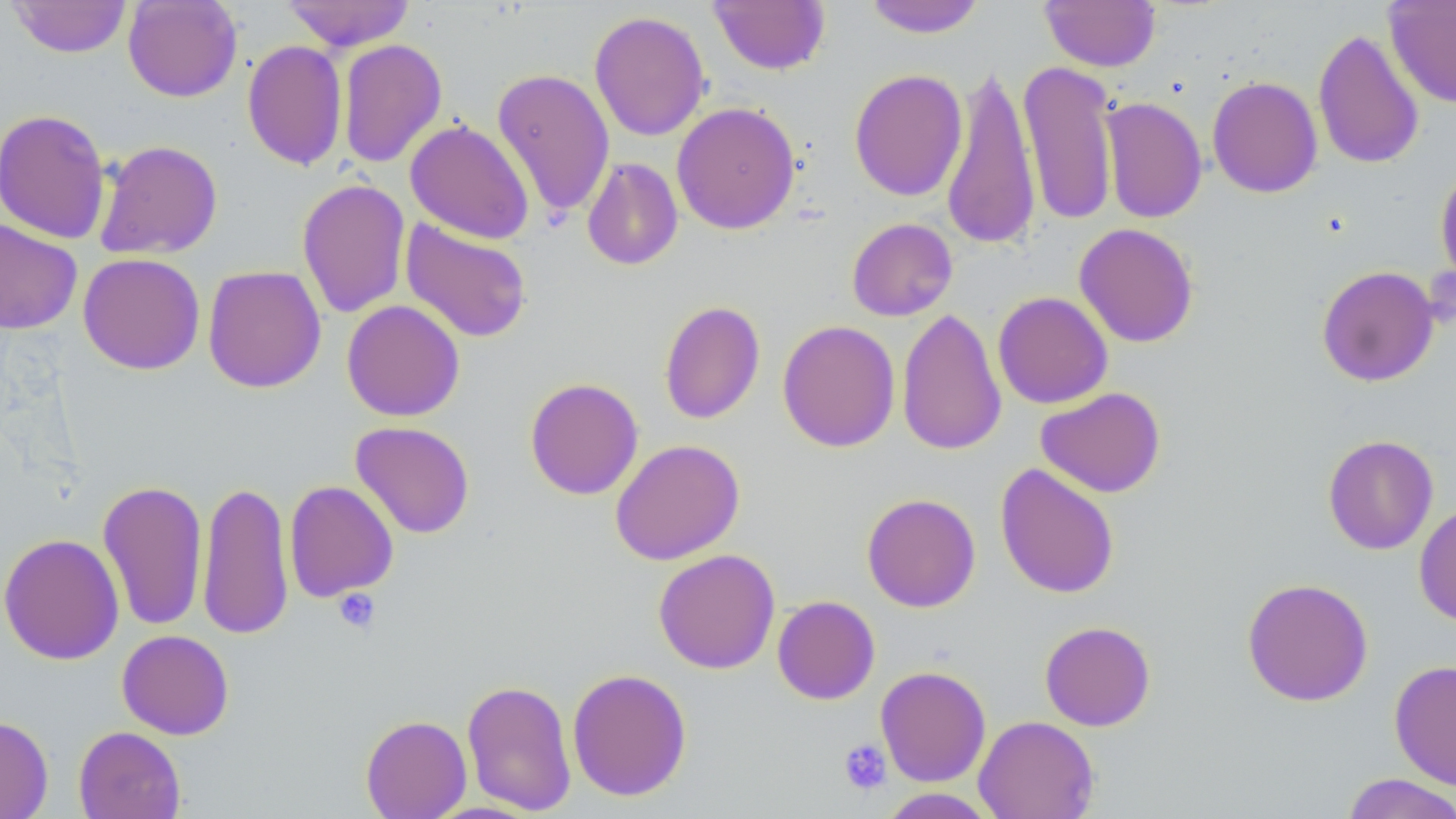 Approximate bounding boxes as (x1, y1, x2, y2) in pixels. Platelet locations: (332, 587, 380, 633), (838, 738, 892, 795). Uninfected red blood cell locations: (8, 0, 132, 58), (122, 0, 242, 102), (282, 0, 415, 51), (862, 0, 987, 38), (1040, 0, 1161, 71), (1384, 0, 1456, 108), (708, 1, 831, 75), (589, 11, 710, 141), (1312, 27, 1425, 170), (337, 38, 447, 169), (242, 40, 348, 171), (1018, 58, 1119, 227), (941, 63, 1041, 251), (492, 67, 615, 221), (848, 68, 967, 201), (1207, 76, 1323, 198), (1100, 96, 1207, 224), (672, 101, 800, 234), (0, 109, 112, 244), (405, 119, 535, 244), (94, 140, 223, 260), (581, 157, 683, 271), (1435, 164, 1456, 290), (297, 178, 411, 319), (846, 217, 958, 322), (0, 218, 83, 334), (400, 218, 533, 344), (1074, 223, 1199, 348), (78, 253, 205, 375), (202, 265, 326, 393), (1316, 265, 1440, 387), (992, 291, 1113, 409), (341, 300, 465, 421), (658, 300, 765, 425), (897, 307, 1007, 456), (777, 320, 900, 453), (524, 377, 644, 500), (1036, 387, 1166, 498), (350, 421, 475, 539), (1323, 434, 1438, 554), (610, 439, 745, 565), (995, 463, 1120, 599), (97, 479, 208, 631), (197, 480, 294, 641), (284, 480, 399, 602), (861, 493, 981, 612), (1414, 503, 1456, 627), (0, 533, 124, 665), (653, 548, 780, 674), (1242, 577, 1373, 707), (772, 595, 880, 705), (1039, 620, 1156, 731), (116, 630, 234, 740), (1389, 660, 1456, 790), (875, 665, 991, 787), (567, 667, 692, 801), (461, 679, 577, 816), (360, 714, 472, 819), (0, 715, 53, 819), (974, 715, 1099, 819), (73, 726, 186, 819), (1340, 773, 1456, 819), (877, 788, 999, 818). Slide-level diagnosis: no evidence of blood parasites. May-Grünwald-Giemsa-stained preparation. Optical microscopy. Thin blood smear. One field of a larger specimen. Captured at 1000x magnification. Image is 1456×819 pixels.